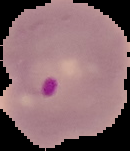

Summary:
  - Malaria status: parasitized
  - Image type: segmented cell region with the area outside set to black
  - Preparation: thin blood smear
  - Image size: 130×151 pixels